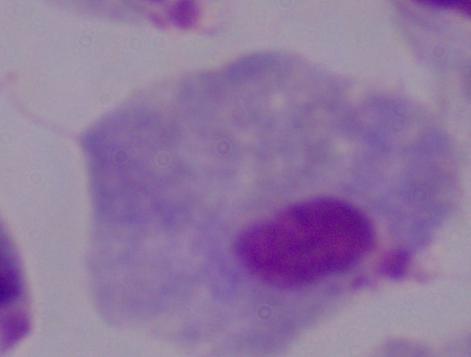
A trichomonad is shown. Photomicrograph. 1000x magnification.